State the blood parasite species.
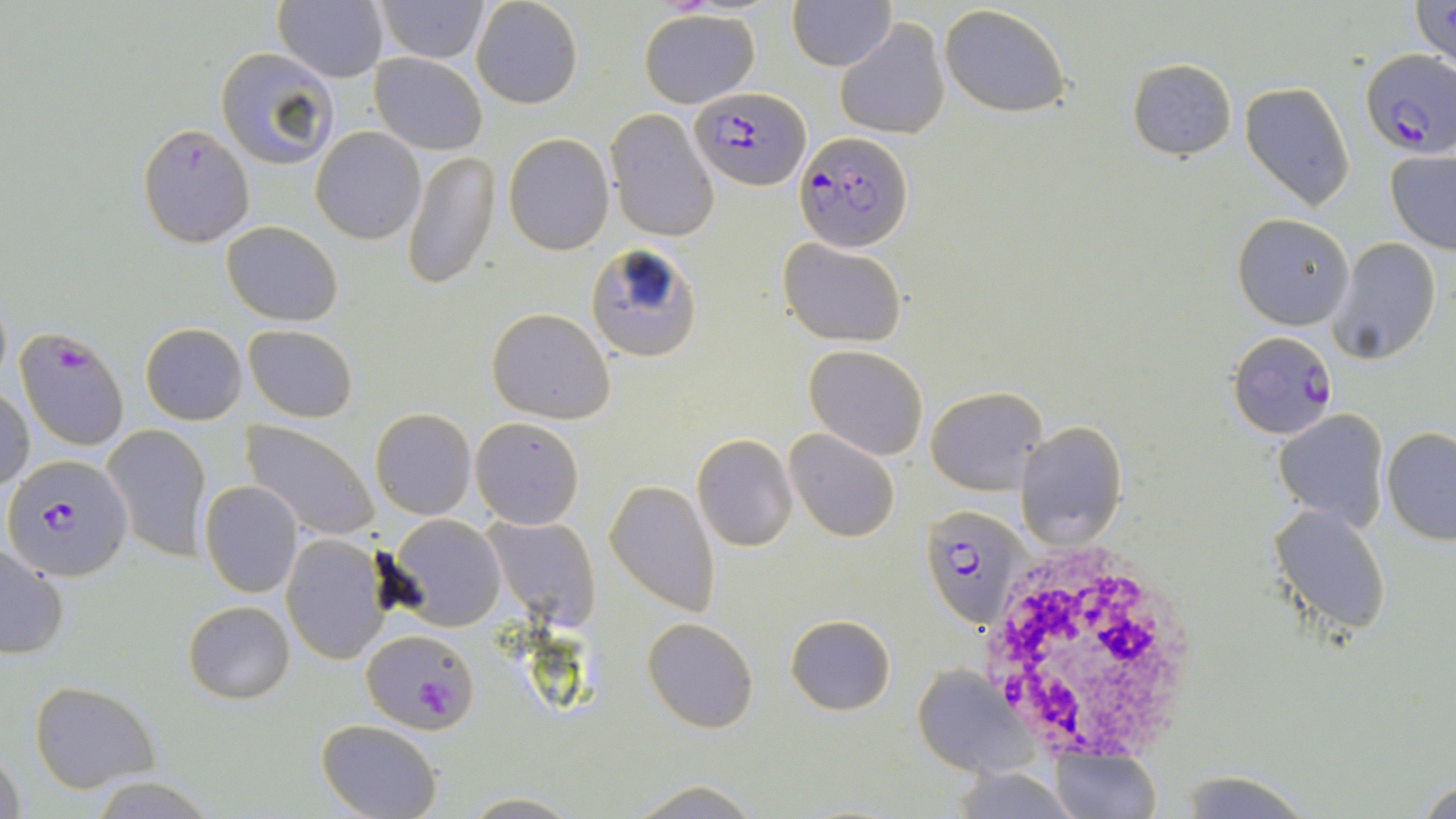

Plasmodium falciparum.

uninfected red blood cell locations = approximate bounding boxes as (x1,y1)-(x2,y2) corner pairs in pixels: (275,0)-(389,83), (373,0)-(491,64), (470,0)-(584,109), (1410,0)-(1455,75), (788,1)-(894,70), (939,5)-(1071,118), (638,9)-(759,108), (835,18)-(951,140), (215,48)-(338,172), (370,54)-(488,155), (1127,57)-(1237,161), (1240,80)-(1356,211), (608,109)-(720,242), (136,123)-(255,248), (311,126)-(426,244), (504,132)-(613,254), (1384,148)-(1456,255), (403,149)-(501,290), (1233,213)-(1354,329), (220,221)-(342,326), (778,239)-(908,346), (1329,239)-(1443,364), (585,242)-(701,360), (486,309)-(616,424), (141,323)-(247,424), (243,324)-(358,422), (803,346)-(929,461), (925,385)-(1047,495), (1,386)-(34,492), (370,408)-(477,521), (1274,408)-(1392,530), (470,417)-(585,530), (241,421)-(379,543), (1016,421)-(1128,549), (103,423)-(210,563), (1381,427)-(1456,545), (786,429)-(901,543), (692,434)-(799,552), (605,479)-(719,616), (199,481)-(304,598), (1270,504)-(1391,638), (387,514)-(506,632), (479,514)-(601,629), (281,535)-(391,664), (0,543)-(69,661), (184,600)-(295,703), (786,615)-(896,715), (643,616)-(759,732), (909,668)-(1035,778), (29,681)-(159,792), (316,718)-(443,819), (0,745)-(24,819), (1049,746)-(1160,819), (945,767)-(1081,819), (92,776)-(214,817), (1418,776)-(1456,818), (621,778)-(771,818), (458,792)-(583,817)
Plasmodium falciparum-infected red blood cell locations = approximate bounding boxes as (x1,y1)-(x2,y2) corner pairs in pixels: (1358,50)-(1456,158), (688,86)-(806,190), (794,130)-(912,251), (13,327)-(131,453), (1228,332)-(1336,438), (4,461)-(128,577), (922,505)-(1028,630), (361,627)-(478,734)
modality = optical microscopy
image size = 1456×819 pixels
stain = May-Grünwald-Giemsa
white blood cell locations = approximate bounding boxes as (x1,y1)-(x2,y2) corner pairs in pixels: (978,546)-(1200,758)
preparation = thin blood smear
magnification = 1000x
field of view = single